Classify this cell by malaria status.
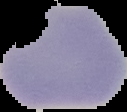
Parasitized.

The area outside the segmented cell region is set to black. Image is 127×112 pixels. From a thin blood smear.